Report the malaria status of this cell.
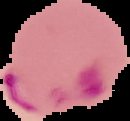

It is parasitized.

Image is 130×121 pixels. From a thin blood film. Cell region segmented out of the field of view; the surrounding area is masked to black.